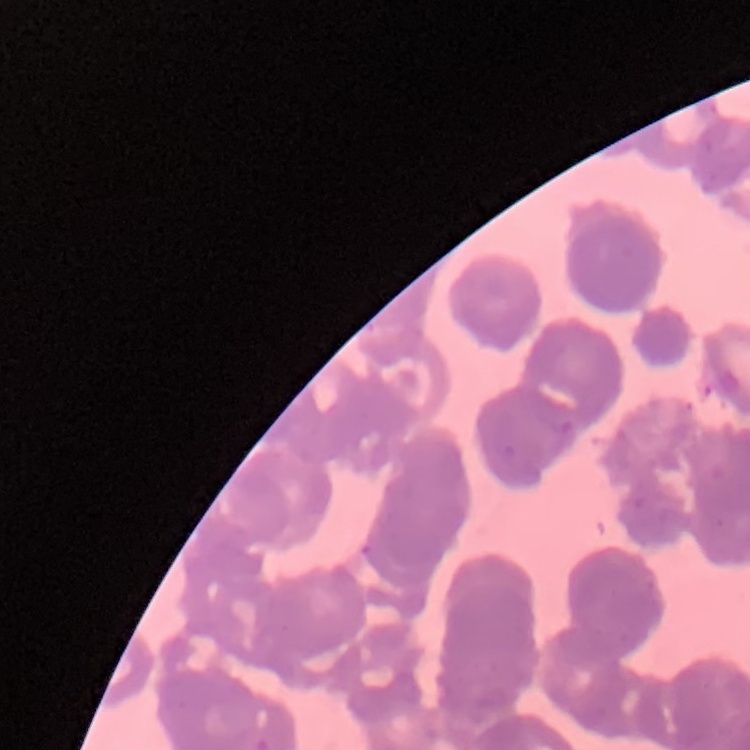

Summary:
  - Red blood cell morphology: rouleaux formation
  - Preparation: thin blood smear
  - Stain: Field's or Giemsa
  - Image type: one tile cut from a larger photomicrograph